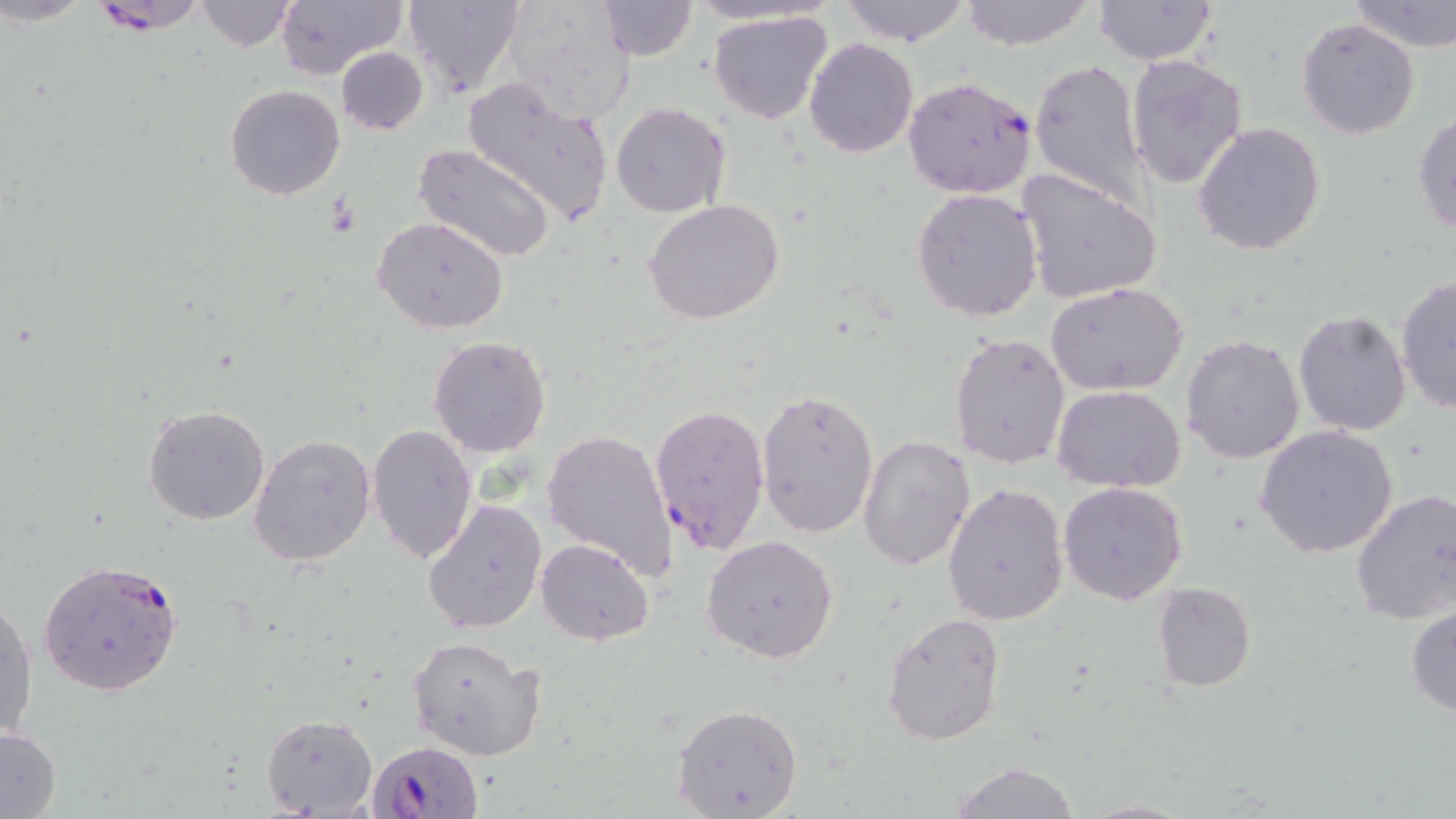

Summary:
  - Coordinate format: approximate bounding boxes as (x1,y1)-(x2,y2) corner pairs in pixels
  - Plasmodium falciparum-infected red blood cell locations: (87,0)-(213,35), (902,76)-(1037,199), (648,403)-(772,555), (36,557)-(183,698), (369,742)-(486,819)
  - Uninfected red blood cell locations: (3,0)-(97,28), (402,0)-(524,99), (494,0)-(640,120), (838,0)-(973,45), (958,0)-(1097,50), (1346,0)-(1456,51), (194,1)-(296,52), (275,1)-(405,80), (594,1)-(697,61), (1093,1)-(1219,67), (706,11)-(835,126), (1296,17)-(1420,139), (804,37)-(919,157), (335,47)-(429,135), (1125,53)-(1250,189), (1029,58)-(1148,207), (460,76)-(616,225), (225,85)-(346,200), (617,94)-(747,315), (611,102)-(729,218), (1411,111)-(1456,235), (1192,121)-(1326,256), (413,142)-(556,262), (1015,168)-(1164,306), (910,188)-(1045,323), (643,198)-(785,325), (373,216)-(510,336), (1394,274)-(1456,414), (1045,283)-(1190,396), (1293,309)-(1413,435), (948,331)-(1070,469), (1180,334)-(1306,465), (427,336)-(552,459), (1052,385)-(1186,493), (756,388)-(879,539), (142,404)-(271,526), (367,424)-(479,565), (1254,424)-(1399,559), (541,428)-(675,581), (248,434)-(376,567), (857,434)-(977,574), (1057,481)-(1189,605), (942,483)-(1070,627), (1349,487)-(1456,626), (422,498)-(548,634), (703,534)-(840,664), (535,538)-(653,645), (1152,581)-(1256,693), (1,595)-(37,745), (1405,605)-(1456,716), (882,611)-(1007,746), (408,635)-(546,761), (671,703)-(804,818), (259,712)-(376,816), (0,727)-(61,816), (948,761)-(1083,819)
  - Slide-level diagnosis: Plasmodium falciparum
  - Field of view: one of a larger specimen
  - Image size: 1456×819 pixels
  - Preparation: thin blood smear
  - Modality: optical microscopy
  - Stain: May-Grünwald-Giemsa
  - Magnification: 1000x